Identify the parasite.
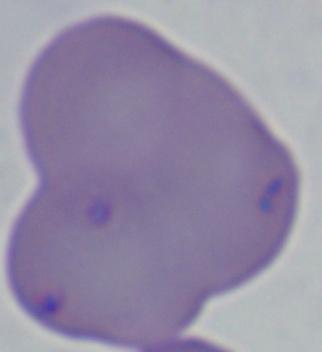

Babesia.

1000x magnification. Photomicrograph.